Assess this cell for malaria.
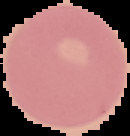
It is uninfected.

Summary:
  - Preparation: thin blood smear
  - Image size: 130×136 pixels
  - Image type: segmented cell region with the area outside set to black